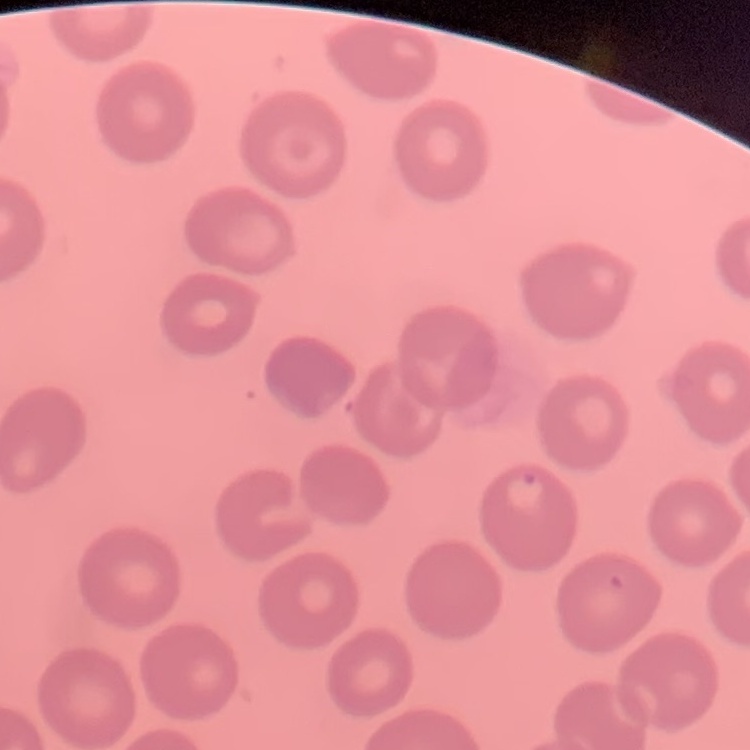

Summary:
  - Red blood cell morphology: no rouleaux formation
  - Preparation: thin blood smear
  - Stain: Field's or Giemsa
  - Image type: square crop of a larger photomicrograph